Identify the parasite.
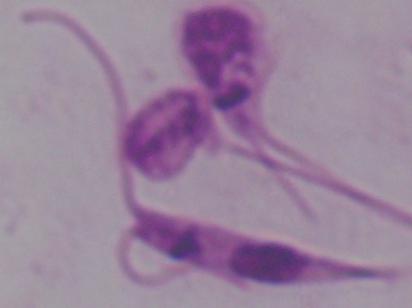
Leishmania.

modality = photomicrograph
magnification = 1000x